Classify this cell by malaria status.
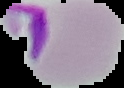

Uninfected.

preparation = thin blood smear
image size = 124×88 pixels
image type = cell region segmented out of the field of view; surrounding area masked to black